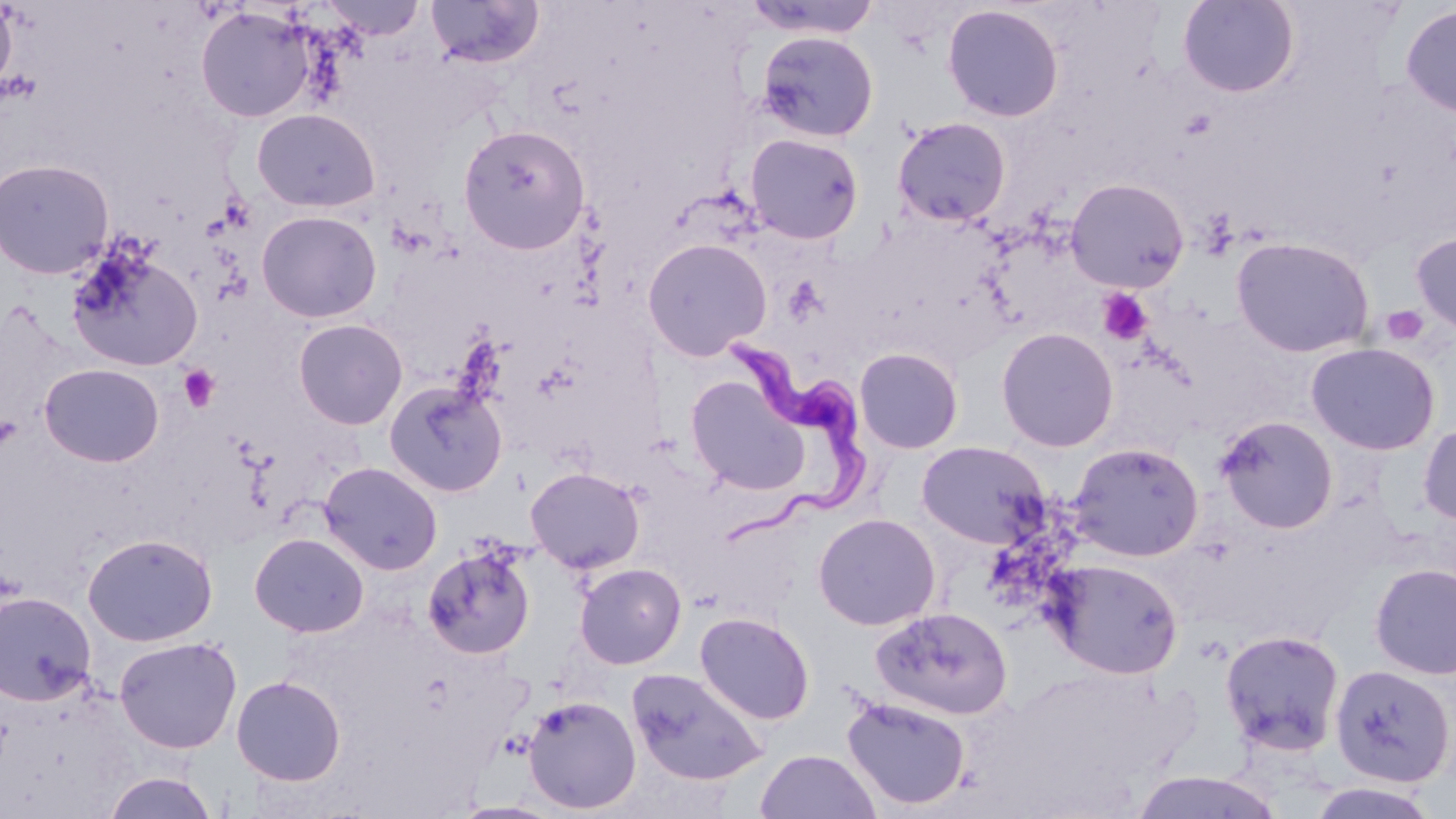
Summary:
  - Coordinate format: approximate bounding boxes as (x1, y1, x2, y2) in pixels
  - Uninfected red blood cell locations: (320, 0, 427, 41), (426, 0, 545, 69), (744, 0, 882, 40), (1177, 0, 1300, 98), (0, 1, 17, 95), (942, 4, 1064, 122), (1399, 4, 1456, 119), (194, 5, 319, 123), (755, 31, 879, 143), (252, 108, 380, 212), (892, 116, 1011, 227), (457, 124, 591, 254), (745, 133, 864, 244), (0, 158, 115, 279), (1065, 177, 1190, 293), (256, 210, 382, 322), (1411, 231, 1456, 336), (1231, 236, 1375, 358), (642, 238, 772, 361), (65, 247, 204, 372), (293, 318, 408, 430), (996, 326, 1119, 452), (1306, 342, 1440, 455), (854, 347, 964, 454), (39, 363, 164, 467), (685, 375, 811, 496), (384, 379, 508, 497), (1215, 415, 1339, 534), (1418, 421, 1456, 525), (916, 440, 1049, 549), (1068, 441, 1204, 562), (319, 462, 443, 575), (526, 467, 645, 574), (813, 513, 940, 631), (82, 532, 218, 647), (249, 533, 369, 638), (422, 542, 536, 659), (1047, 558, 1183, 678), (574, 562, 686, 669), (1369, 563, 1456, 679), (0, 591, 97, 707), (872, 606, 1013, 720), (694, 611, 815, 725), (1220, 629, 1346, 757), (114, 636, 242, 753), (1329, 663, 1454, 787), (626, 666, 768, 786), (231, 675, 346, 785), (522, 695, 641, 814), (841, 696, 971, 810), (755, 749, 882, 819), (1127, 770, 1286, 818), (101, 771, 220, 819), (1305, 781, 1443, 818)
  - Platelet locations: (1097, 287, 1154, 345), (1381, 305, 1429, 346), (178, 364, 221, 412)
  - Trypanosoma brucei locations: (708, 333, 877, 548)
  - Slide-level diagnosis: Trypanosoma brucei
  - Magnification: 1000x
  - Modality: optical microscopy
  - Field of view: one of a larger specimen
  - Image size: 1456×819 pixels
  - Preparation: thin blood film
  - Stain: May-Grünwald-Giemsa